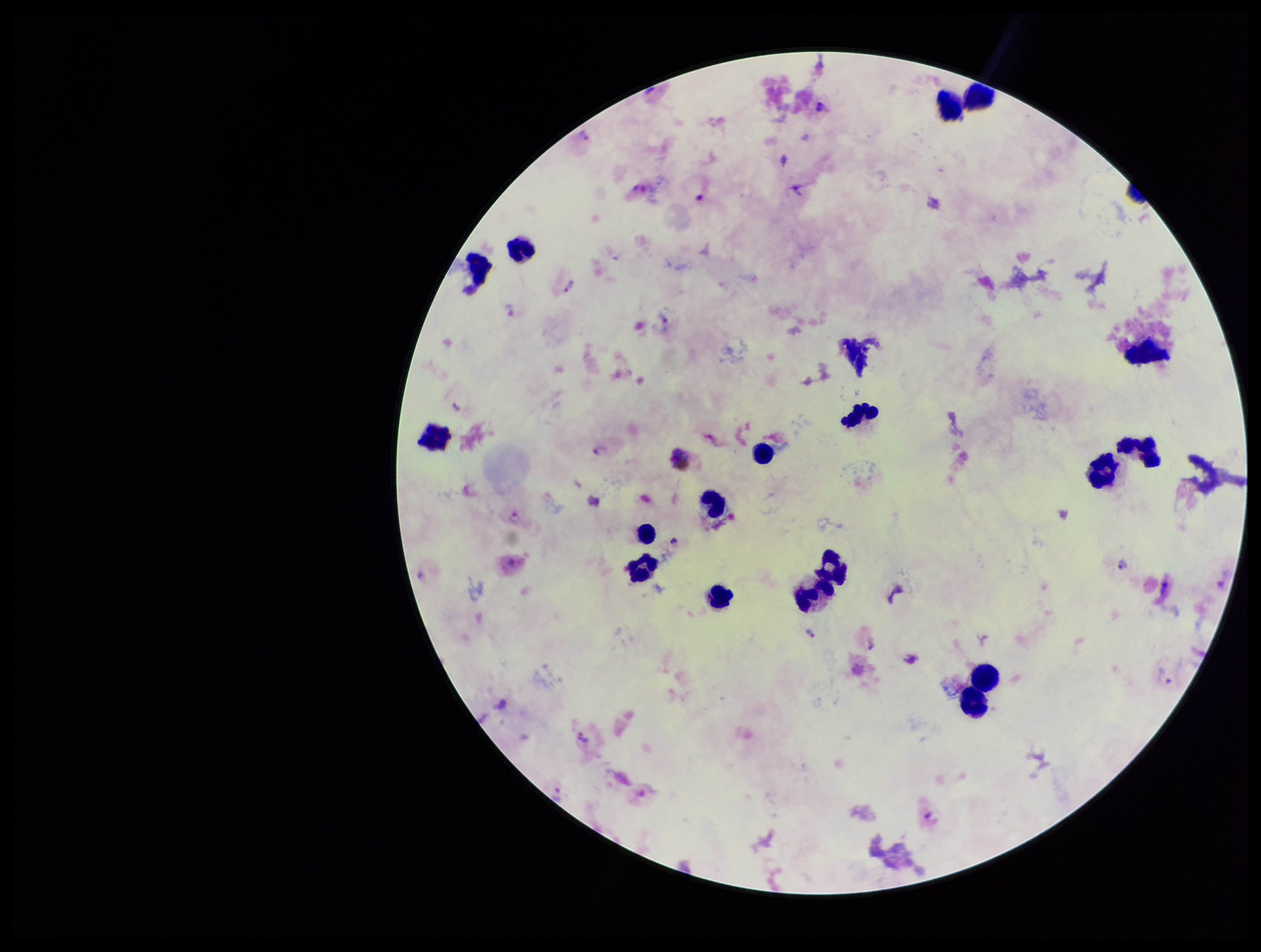 Patient malaria status: positive. One field from this slide. Stained with Giemsa. Image is 1261×952 pixels. Parasite count: 16. Smartphone photograph taken through the eyepiece of a microscope. Preparation: thick. Leukocyte count: 19. Species reported for this patient: Plasmodium vivax. Plasmodium parasites: detected.